Outline each white blood cell.
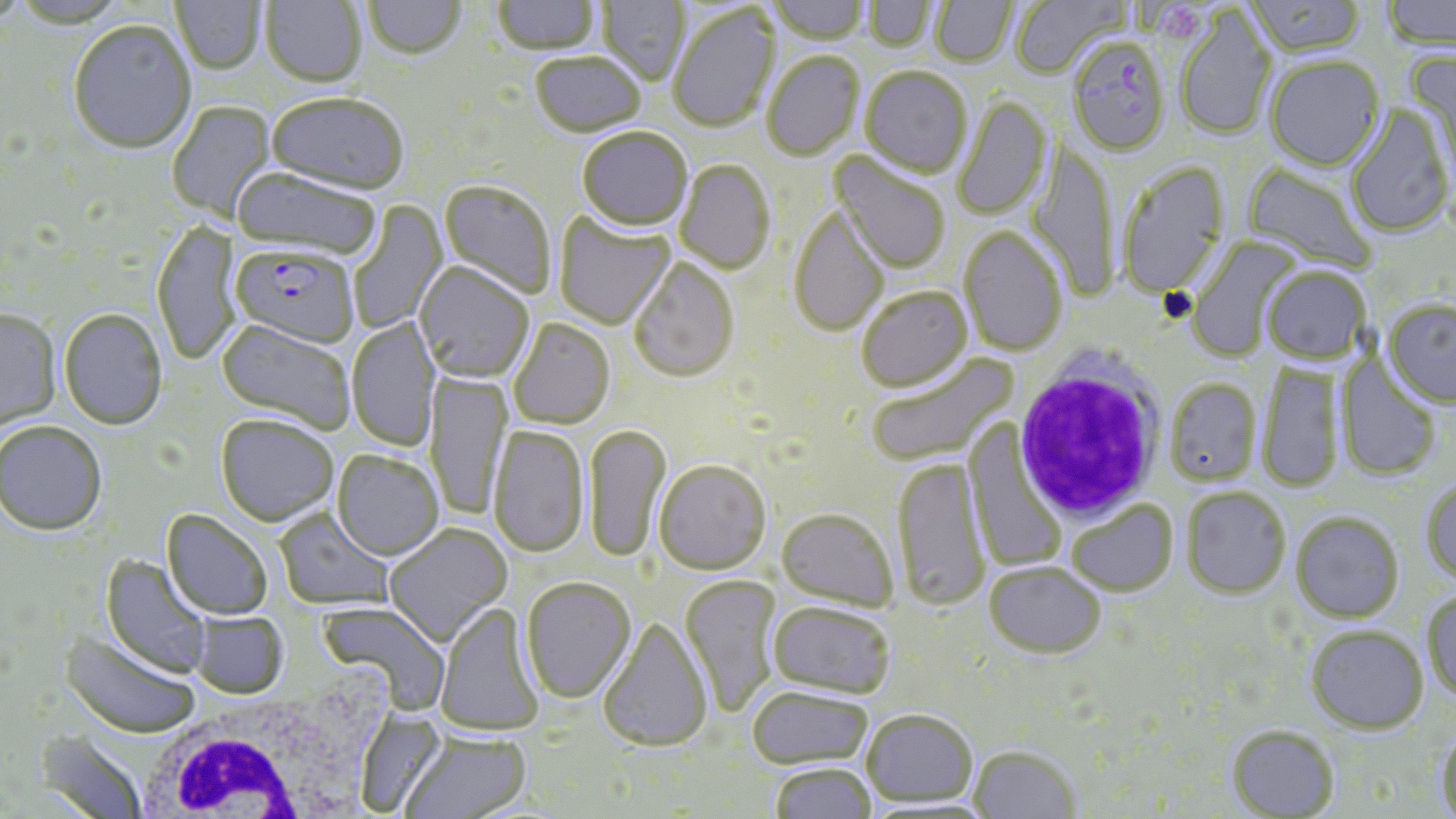

Approximate bounding boxes as [x1, y1, x2, y2] in pixels.
White blood cells: [1013, 356, 1165, 522], [141, 698, 373, 817].

slide-level diagnosis = Plasmodium falciparum
magnification = 1000x
platelet locations = approximate bounding boxes as [x1, y1, x2, y2] in pixels: [1159, 4, 1201, 39]
modality = optical microscopy
preparation = thin blood film
field of view = one of a larger specimen
Plasmodium falciparum-infected red blood cell locations = approximate bounding boxes as [x1, y1, x2, y2] in pixels: [1067, 39, 1171, 158], [230, 247, 359, 351]
image size = 1456×819 pixels
stain = May-Grünwald-Giemsa
uninfected red blood cell locations = approximate bounding boxes as [x1, y1, x2, y2] in pixels: [171, 0, 265, 76], [261, 0, 366, 90], [493, 0, 601, 57], [597, 0, 690, 87], [768, 0, 869, 46], [863, 0, 938, 53], [931, 0, 1017, 69], [1011, 0, 1127, 80], [1245, 0, 1366, 58], [1381, 0, 1456, 53], [364, 1, 465, 63], [668, 4, 782, 135], [1175, 7, 1278, 142], [68, 22, 196, 158], [1404, 45, 1456, 194], [762, 53, 864, 162], [530, 54, 646, 140], [1266, 57, 1384, 172], [860, 68, 973, 180], [267, 95, 407, 199], [954, 96, 1052, 221], [168, 101, 277, 223], [1346, 105, 1456, 238], [577, 129, 692, 234], [1027, 141, 1118, 302], [829, 151, 950, 275], [675, 161, 775, 275], [1117, 161, 1231, 299], [1242, 163, 1378, 275], [230, 168, 380, 263], [439, 180, 556, 300], [349, 200, 449, 334], [789, 206, 890, 338], [554, 210, 675, 331], [152, 221, 241, 368], [959, 226, 1067, 357], [1185, 237, 1300, 362], [629, 258, 739, 384], [414, 264, 534, 385], [1262, 266, 1371, 366], [856, 286, 973, 392], [1383, 299, 1456, 406], [0, 311, 61, 432], [59, 311, 168, 431], [347, 316, 441, 453], [509, 319, 615, 430], [215, 320, 355, 436], [866, 352, 1018, 469], [1336, 353, 1443, 482], [1257, 366, 1342, 493], [425, 370, 512, 521], [1165, 378, 1262, 486], [216, 417, 339, 528], [964, 420, 1066, 573], [0, 423, 107, 538], [585, 424, 672, 564], [488, 427, 590, 559], [332, 451, 444, 562], [895, 457, 988, 611], [654, 460, 771, 575], [1420, 478, 1456, 587], [1182, 486, 1291, 598], [1066, 499, 1178, 597], [777, 507, 899, 612], [274, 508, 397, 612], [161, 511, 273, 622], [1291, 511, 1404, 622], [385, 525, 513, 647], [101, 555, 213, 680], [985, 561, 1106, 658], [680, 575, 782, 718], [521, 579, 636, 704], [1422, 591, 1456, 703], [319, 601, 452, 714], [769, 601, 896, 700], [433, 602, 545, 738], [191, 612, 288, 699], [598, 616, 713, 753], [1306, 624, 1428, 733], [60, 630, 199, 739], [747, 686, 875, 769], [862, 708, 978, 807], [354, 709, 450, 816], [1227, 725, 1340, 818], [1436, 728, 1456, 817], [34, 730, 150, 819], [399, 732, 531, 819], [969, 744, 1082, 819], [771, 762, 877, 819]